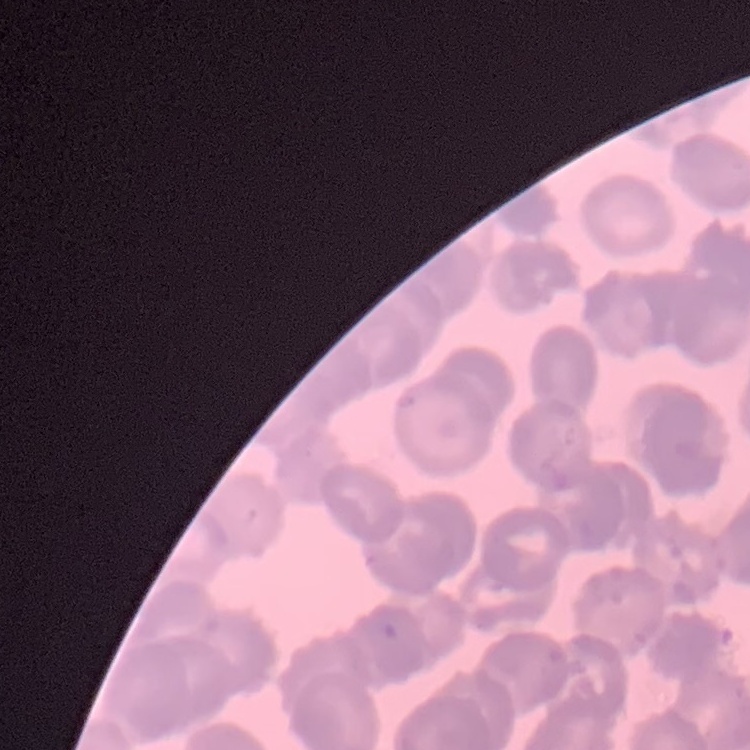

erythrocyte morphology = rouleaux formation
preparation = thin blood smear
image type = one tile cut from a larger photomicrograph
stain = Field's or Giemsa